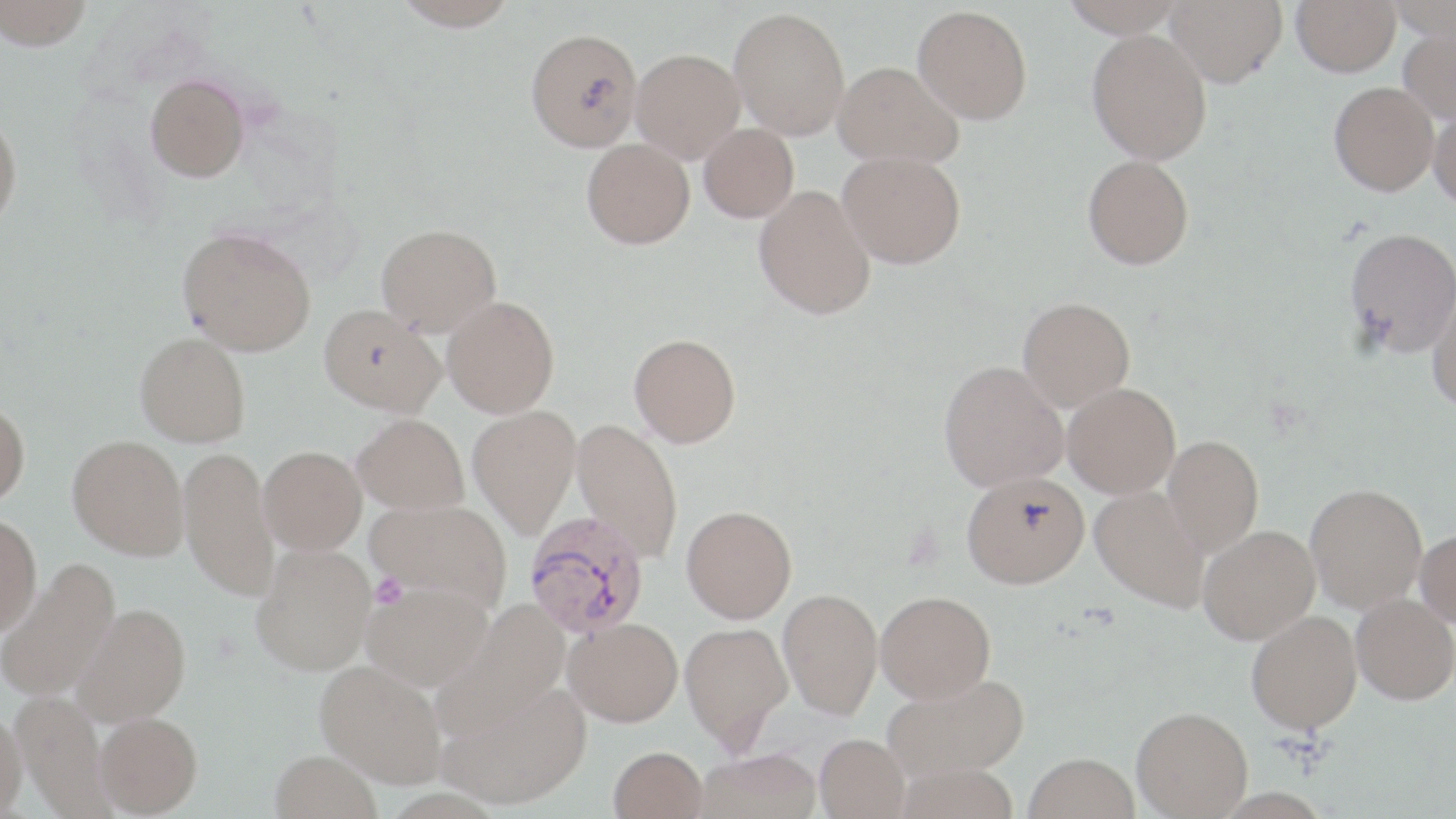
{
  "slide_level_diagnosis": "Plasmodium vivax",
  "field_of_view": "single",
  "uninfected_red_blood_cell_locations": "approximate bounding boxes as (x1,y1)-(x2,y2) corner pairs in pixels: (0,0)-(94,51), (391,0)-(520,32), (1060,0)-(1186,38), (1165,0)-(1287,87), (1291,0)-(1400,76), (1388,0)-(1456,41), (912,5)-(1033,124), (728,7)-(850,139), (1398,24)-(1456,125), (525,28)-(644,151), (1087,29)-(1212,164), (631,48)-(745,162), (833,61)-(963,168), (145,74)-(249,182), (1329,81)-(1438,196), (1429,106)-(1456,210), (0,111)-(23,231), (698,123)-(799,222), (582,138)-(695,249), (838,150)-(967,268), (1082,155)-(1194,269), (753,184)-(876,320), (376,223)-(502,336), (177,226)-(316,356), (1344,226)-(1456,357), (1427,283)-(1456,414), (442,295)-(560,418), (1018,296)-(1136,412), (318,305)-(445,416), (135,332)-(251,446), (629,333)-(741,447), (938,360)-(1068,491), (1063,382)-(1181,498), (0,401)-(30,508), (468,405)-(581,538), (353,413)-(469,515), (571,419)-(684,563), (1162,434)-(1264,556), (67,435)-(189,560), (179,445)-(278,601), (259,445)-(367,554), (962,471)-(1090,588), (1305,483)-(1428,614), (1090,485)-(1210,611), (366,500)-(513,610), (681,504)-(797,623), (0,514)-(42,636), (1198,524)-(1321,644), (1415,529)-(1456,628), (252,544)-(376,675), (0,559)-(120,703), (361,583)-(493,690), (778,587)-(883,720), (876,590)-(996,703), (1351,593)-(1456,705), (72,603)-(191,725), (431,603)-(571,741), (1247,610)-(1362,732), (564,617)-(683,726), (680,622)-(792,752), (315,660)-(447,787), (883,673)-(1029,781), (437,680)-(592,810), (11,690)-(112,819), (1131,706)-(1252,818), (0,708)-(27,818), (95,712)-(203,817), (815,733)-(910,819), (609,746)-(708,819), (695,748)-(822,819), (270,749)-(382,819), (1024,753)-(1139,819)",
  "stain": "May-Grünwald-Giemsa",
  "magnification": "1000x",
  "modality": "light microscopy",
  "preparation": "thin blood smear",
  "platelet_locations": "approximate bounding boxes as (x1,y1)-(x2,y2) corner pairs in pixels: (370,573)-(408,609)",
  "image_size": "1456×819 pixels",
  "plasmodium_vivax_infected_red_blood_cell_locations": "approximate bounding boxes as (x1,y1)-(x2,y2) corner pairs in pixels: (524,511)-(651,639)"
}